Locate and identify every blood parasite.
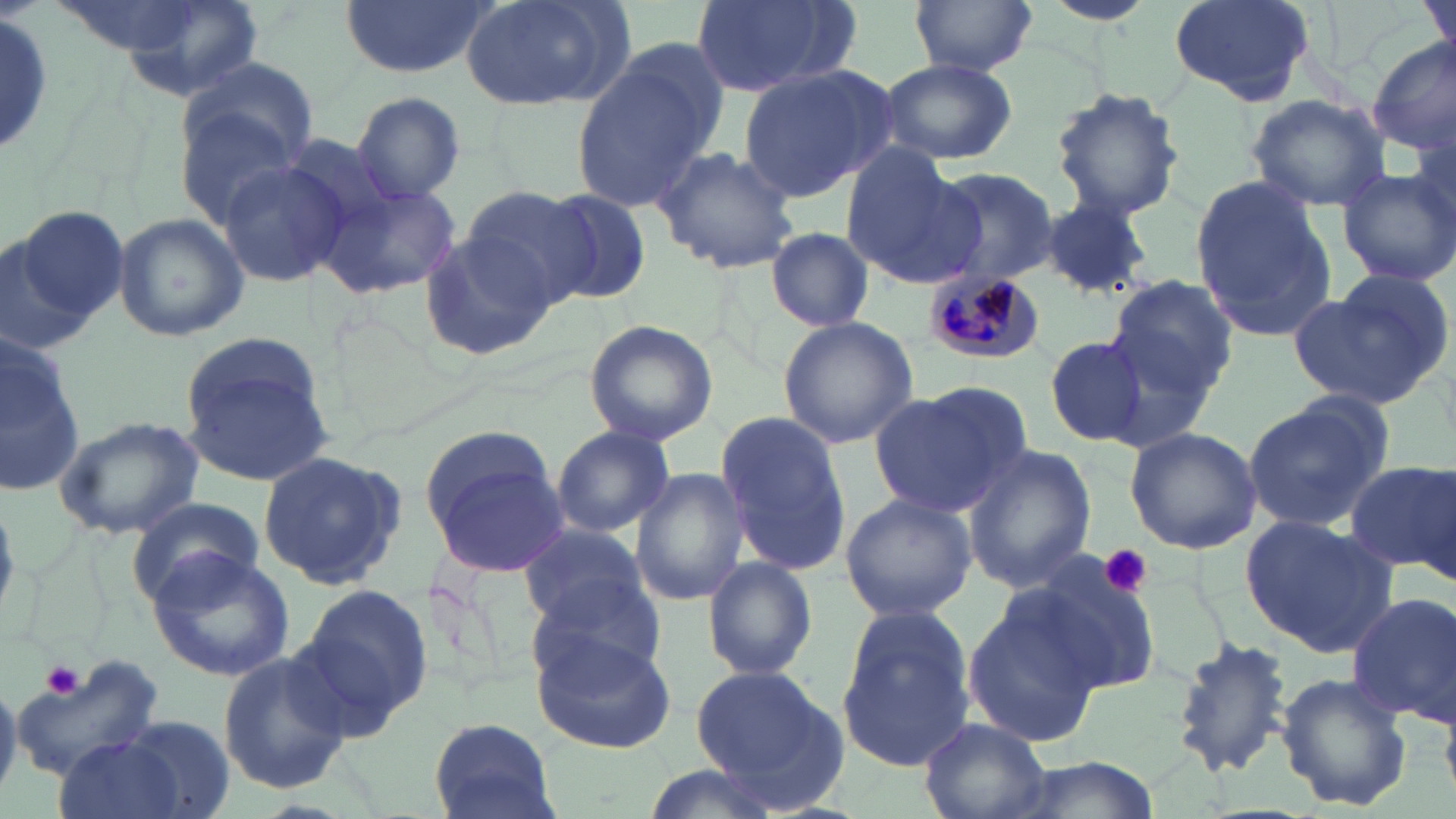
Approximate bounding boxes as (x1,y1)-(x2,y2) corner pairs in pixels.
Plasmodium malariae-infected red blood cells: (922,269)-(1044,360).
No Plasmodium falciparum, Plasmodium ovale, Plasmodium vivax, Babesia divergens, or Trypanosoma brucei observed.

Summary:
  - Platelet locations: (1097,544)-(1153,598), (42,658)-(84,697)
  - Uninfected red blood cell locations: (116,0)-(265,104), (343,0)-(495,79), (459,0)-(629,111), (689,0)-(861,101), (910,0)-(1037,76), (1169,0)-(1316,107), (1421,0)-(1455,69), (1041,1)-(1158,27), (0,12)-(59,160), (1367,37)-(1456,155), (875,56)-(1018,165), (570,57)-(720,211), (738,64)-(893,203), (178,67)-(317,209), (1050,86)-(1186,221), (351,91)-(465,203), (1244,92)-(1390,212), (654,147)-(800,274), (841,148)-(981,287), (215,157)-(350,286), (932,169)-(1062,285), (1337,169)-(1456,285), (1190,173)-(1339,344), (319,178)-(461,300), (459,185)-(597,308), (540,189)-(653,305), (1039,197)-(1157,297), (8,204)-(128,336), (113,212)-(250,342), (766,228)-(875,332), (0,230)-(84,355), (419,232)-(558,361), (1105,276)-(1239,400), (1290,280)-(1446,410), (777,315)-(918,448), (582,319)-(719,445), (1043,333)-(1153,449), (179,334)-(339,485), (0,342)-(88,496), (868,384)-(1032,519), (1242,397)-(1392,533), (713,408)-(853,579), (55,416)-(204,540), (550,426)-(673,538), (1124,427)-(1261,554), (424,436)-(566,576), (963,445)-(1096,592), (255,450)-(407,589), (1346,460)-(1455,575), (631,467)-(750,606), (839,489)-(979,626), (131,499)-(263,599), (1241,516)-(1398,653), (518,521)-(652,630), (147,551)-(295,681), (1019,555)-(1166,699), (702,556)-(817,680), (524,579)-(668,698), (293,584)-(436,735), (1346,592)-(1456,723), (962,599)-(1102,746), (837,610)-(978,771), (532,630)-(679,754), (1171,638)-(1294,778), (218,648)-(351,794), (7,653)-(158,780), (689,664)-(845,797), (1276,672)-(1412,814), (114,717)-(235,819), (427,718)-(561,819), (919,718)-(1051,819), (51,736)-(194,819), (996,754)-(1158,819), (635,763)-(789,819)
  - Slide-level diagnosis: Plasmodium malariae
  - Magnification: 1000x
  - Preparation: thin blood smear
  - Field of view: one of a larger specimen
  - Stain: May-Grünwald-Giemsa
  - Modality: optical microscopy
  - Image size: 1456×819 pixels